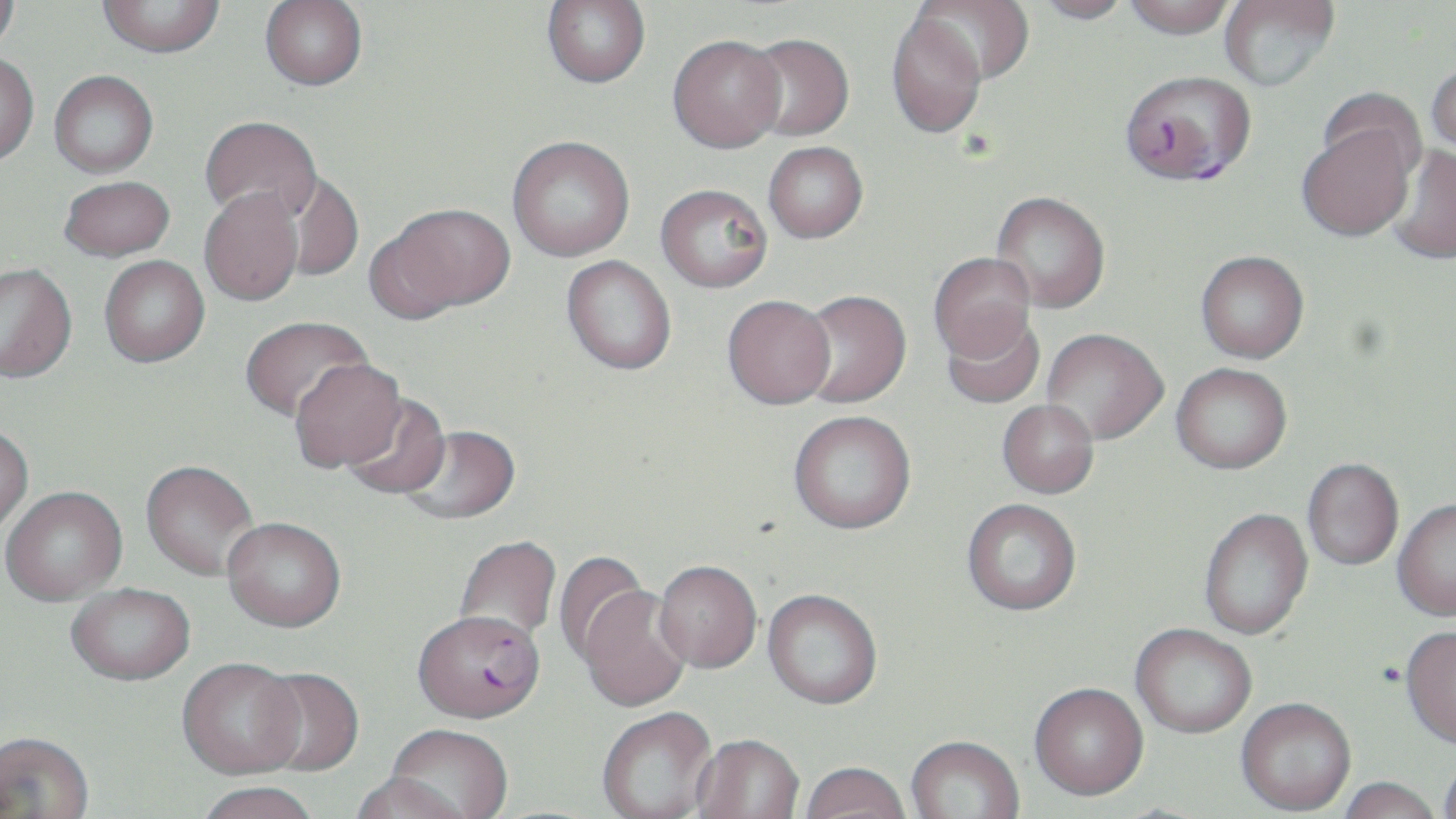
plasmodium_falciparum_infected_red_blood_cell_locations: 'approximate bounding boxes as (x1,y1)-(x2,y2) corner pairs in pixels: (1121,68)-(1253,186), (412,615)-(545,729)'
slide_level_diagnosis: Plasmodium falciparum
modality: optical microscopy
magnification: 1000x
field_of_view: single
image_size: 1456×819 pixels
stain: May-Grünwald-Giemsa
preparation: thin blood film
uninfected_red_blood_cell_locations: 'approximate bounding boxes as (x1,y1)-(x2,y2) corner pairs in pixels: (0,0)-(20,53), (98,0)-(225,57), (541,0)-(651,87), (912,0)-(1035,84), (1030,0)-(1135,25), (1123,0)-(1237,38), (1219,0)-(1340,92), (260,1)-(368,90), (886,12)-(987,139), (743,33)-(854,141), (668,34)-(786,153), (0,53)-(39,165), (1426,60)-(1456,159), (49,70)-(158,177), (1318,87)-(1427,185), (199,115)-(322,225), (1296,120)-(1418,242), (507,135)-(635,261), (763,141)-(868,243), (1387,145)-(1456,264), (279,172)-(363,281), (58,175)-(175,261), (655,183)-(772,293), (199,187)-(304,306), (990,191)-(1110,313), (380,202)-(516,316), (1195,250)-(1309,363), (928,252)-(1036,362), (99,255)-(209,367), (561,255)-(677,375), (0,263)-(77,383), (796,289)-(911,407), (722,295)-(836,409), (940,312)-(1045,410), (239,315)-(374,424), (1042,328)-(1168,444), (289,358)-(408,474), (1171,362)-(1292,474), (341,393)-(452,500), (997,399)-(1099,497), (788,410)-(916,533), (0,426)-(33,538), (400,427)-(521,527), (1302,458)-(1403,570), (140,463)-(260,583), (1,489)-(128,608), (1393,498)-(1456,621), (962,499)-(1082,617), (1199,507)-(1313,640), (222,521)-(346,637), (454,536)-(561,644), (553,552)-(652,666), (654,562)-(761,674), (66,586)-(196,690), (576,586)-(691,714), (762,589)-(882,711), (1130,625)-(1256,739), (1400,627)-(1456,749), (177,662)-(307,783), (253,668)-(364,779), (1029,684)-(1148,803), (1236,698)-(1356,816), (597,710)-(718,819), (384,727)-(513,819), (0,735)-(96,819), (691,737)-(804,819), (906,738)-(1024,819), (1438,755)-(1456,819), (800,765)-(910,819), (348,776)-(471,819), (1337,777)-(1443,819), (194,785)-(320,819)'